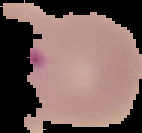

Result: Plasmodium parasites detected. Image is 142×133 pixels. From a thin blood smear. Segmented cell region on a black background.